Report the malaria status of this cell.
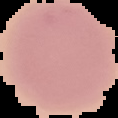

Uninfected.

Summary:
  - Image size: 118×118 pixels
  - Preparation: thin blood film
  - Image type: cell region segmented out of the field of view; surrounding area masked to black